Locate every malaria parasite.
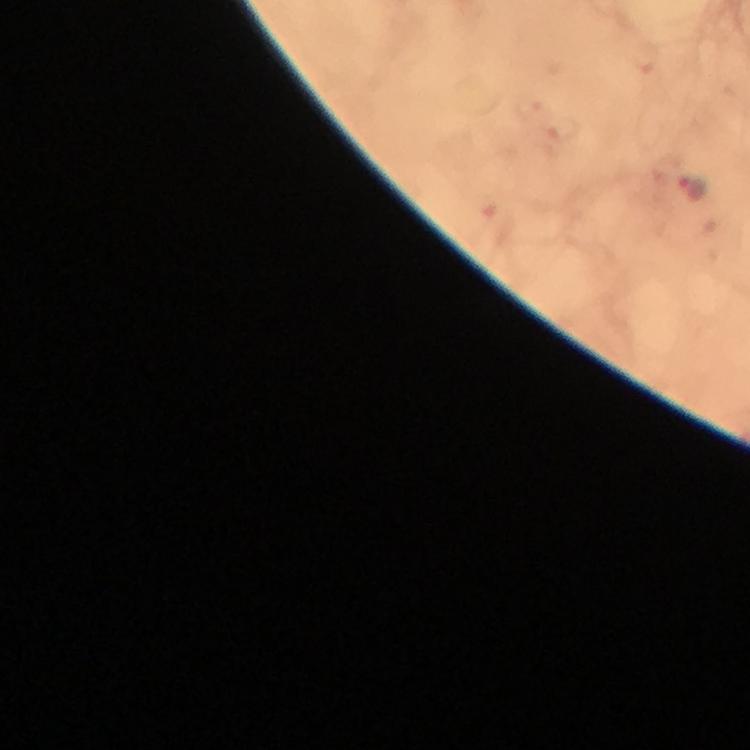
Approximate centers as {x, y} in pixels.
Malaria parasites: {692, 188}.

Immersion oil applied. From a diagnostic examination for malaria. Photographed with a smartphone mounted on the microscope. Image is 750×750 pixels. Giemsa stain. Thick blood smear. At 100x magnification. A crop from one field of view.